State the preparation type.
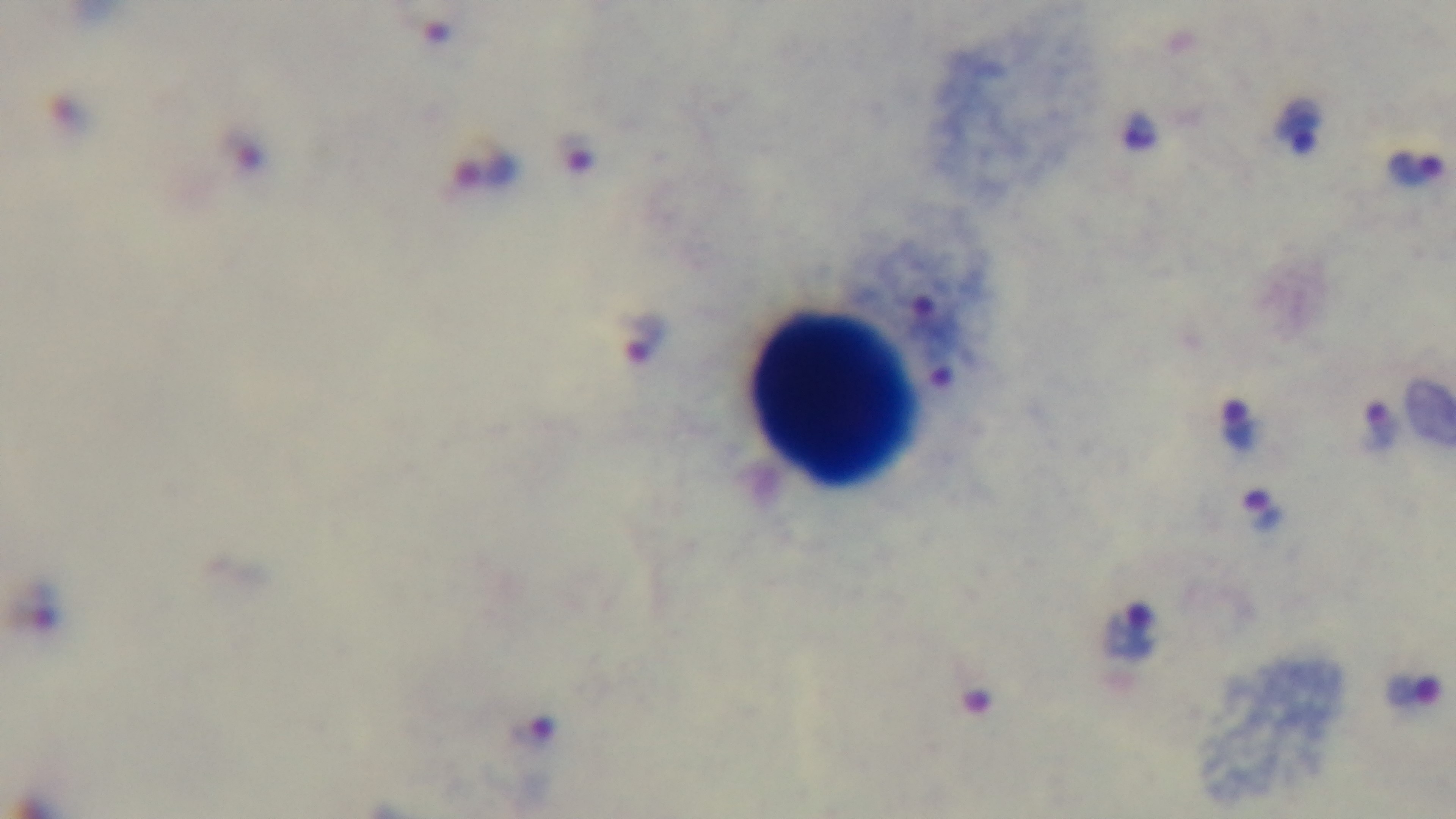
A thick smear.

stain = Giemsa
field of view = one from the slide
capture = mounted 4K digital camera
modality = light microscopy
objective = 100x oil immersion
malaria status = infected